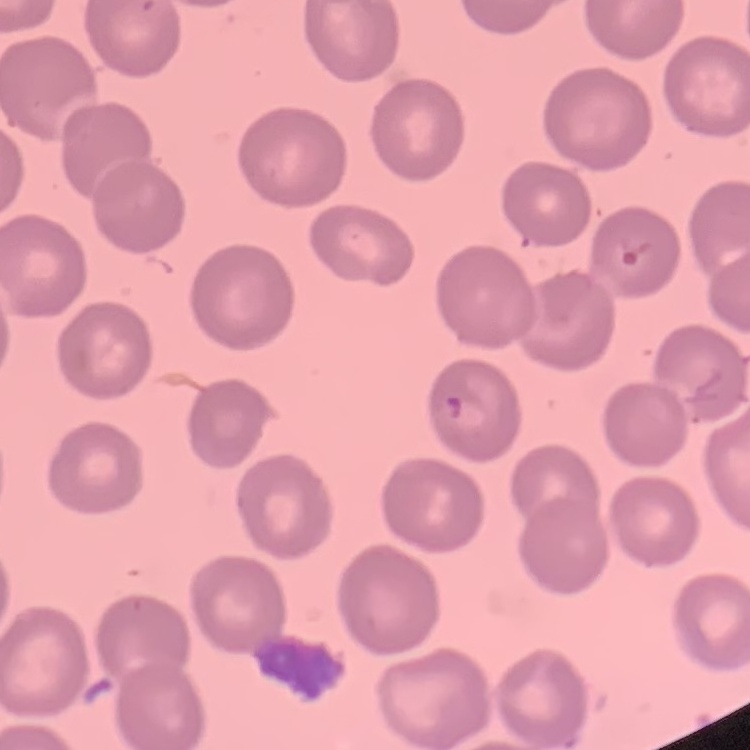 The red blood cells show no rouleaux formation. Stained with either Field's or Giemsa. One tile cut from a larger photomicrograph. Thin peripheral smear.